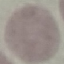
Summary:
  - Result: no malaria parasites seen
  - Preparation: thin blood smear
  - Image type: automatically extracted cell patch, resized to 64 × 64 pixels
  - Capture: smartphone through the microscope eyepiece
  - Stain: Giemsa